Report the malaria status of this cell.
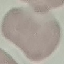

Uninfected.

Automatically extracted cell patch, resized to 64 × 64 pixels. Acquired by smartphone through the microscope eyepiece. Giemsa stain. Thin blood smear.